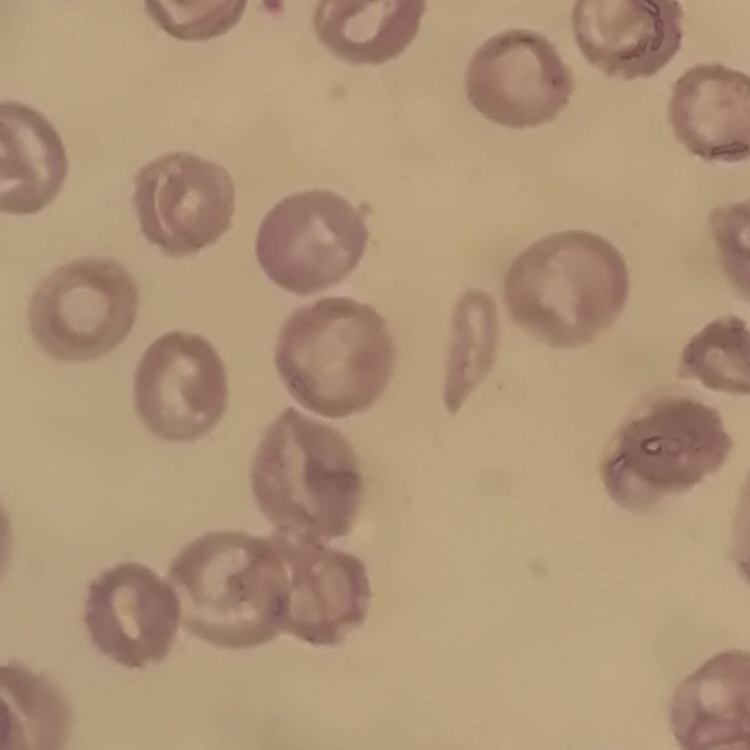

Summary:
  - Red blood cell morphology: no rouleaux formation
  - Stain: Field's or Giemsa
  - Image type: square crop of a larger photomicrograph
  - Preparation: thin blood film